Locate every Plasmodium parasite and every leukocyte.
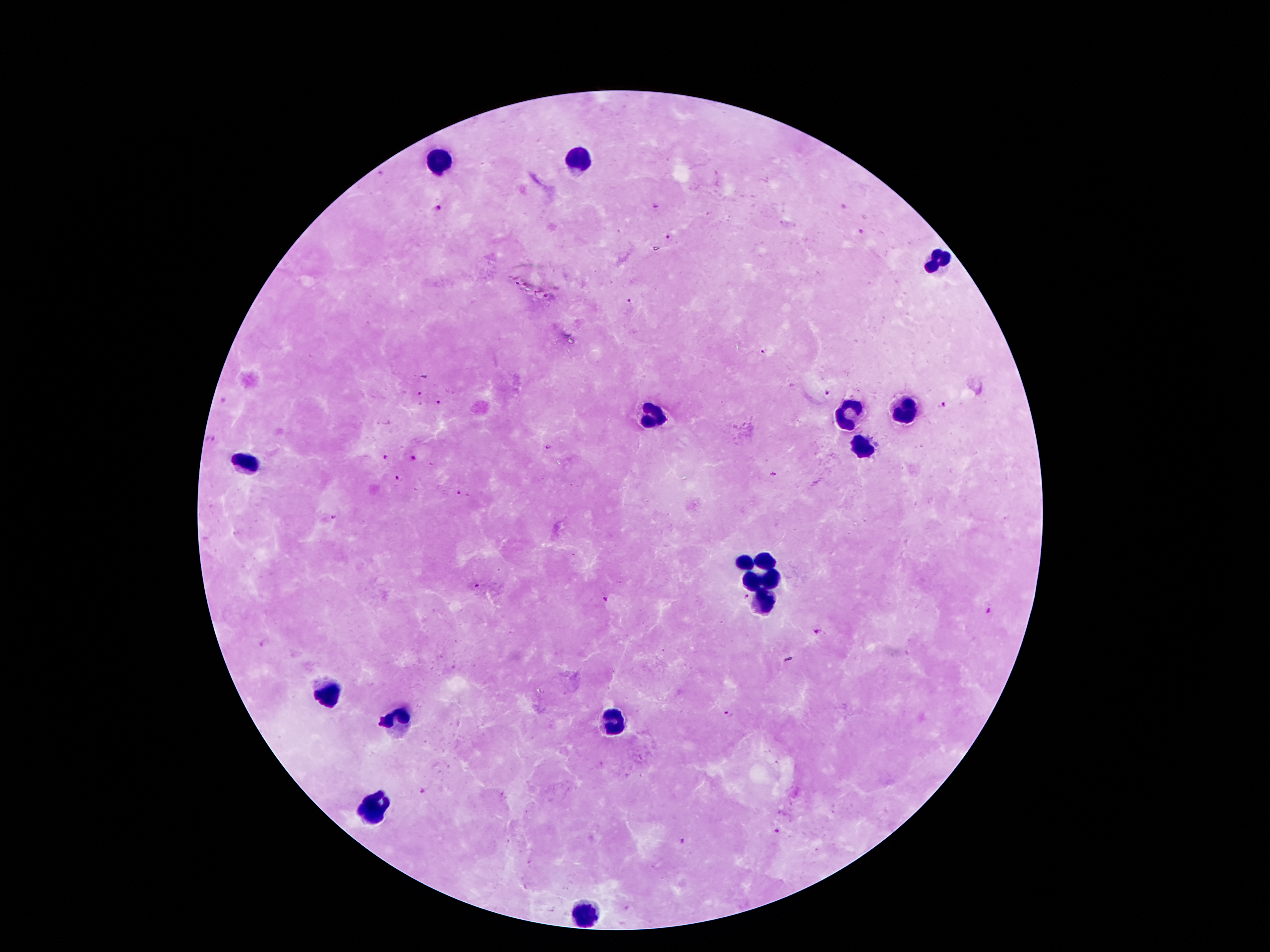
Approximate object centers, in pixels from the top-left corner.
Plasmodium parasites: (x=438, y=208), (x=656, y=208), (x=860, y=232), (x=668, y=237), (x=629, y=301), (x=765, y=353), (x=828, y=392), (x=421, y=394), (x=439, y=402), (x=942, y=404), (x=211, y=439), (x=548, y=448), (x=384, y=458), (x=413, y=460), (x=773, y=475), (x=398, y=478), (x=458, y=494), (x=335, y=516), (x=478, y=585), (x=745, y=596), (x=606, y=599), (x=988, y=611), (x=818, y=631), (x=262, y=643), (x=728, y=714), (x=777, y=831), (x=681, y=841).
Leukocytes: (x=437, y=160), (x=580, y=160), (x=936, y=260), (x=646, y=410), (x=907, y=410), (x=852, y=415), (x=861, y=449), (x=248, y=462), (x=768, y=560), (x=739, y=562), (x=748, y=580), (x=771, y=583), (x=764, y=601), (x=328, y=689), (x=611, y=720), (x=397, y=721), (x=376, y=806), (x=589, y=915).

Summary:
  - Preparation: thick peripheral-blood smear
  - Patient malaria status: positive for Plasmodium falciparum
  - Magnification: 100x
  - Image size: 1270×952 pixels
  - Field of view: single
  - Capture: smartphone through the microscope eyepiece
  - Stain: Giemsa